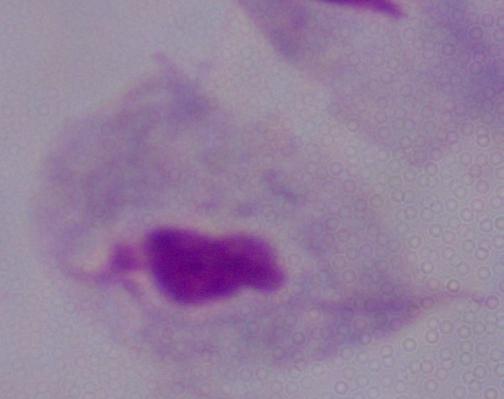
A trichomonad is seen. Captured at 1000x magnification. Micrograph.